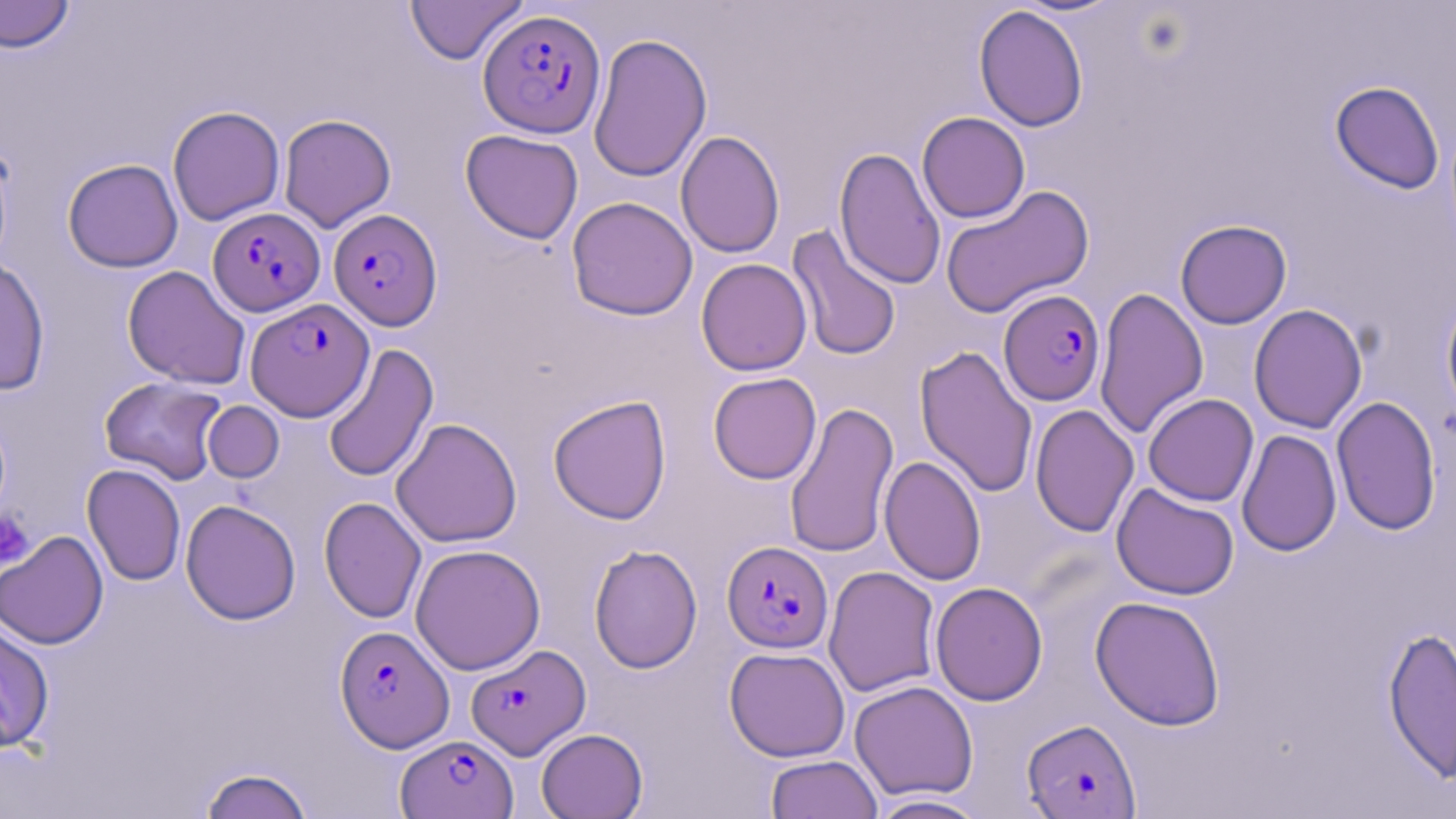 Approximate bounding boxes as named x1/y1/x2/y2 corners in pixels. Plasmodium falciparum-infected red blood cell locations: (x1=478, y1=8, x2=606, y2=138), (x1=208, y1=207, x2=325, y2=316), (x1=328, y1=208, x2=442, y2=330), (x1=998, y1=289, x2=1106, y2=406), (x1=246, y1=298, x2=374, y2=420), (x1=722, y1=540, x2=833, y2=653), (x1=335, y1=625, x2=454, y2=751), (x1=466, y1=644, x2=591, y2=760), (x1=1021, y1=718, x2=1141, y2=818), (x1=395, y1=734, x2=518, y2=819). Uninfected red blood cell locations: (x1=405, y1=0, x2=528, y2=65), (x1=0, y1=1, x2=75, y2=53), (x1=973, y1=5, x2=1088, y2=132), (x1=588, y1=33, x2=712, y2=182), (x1=1330, y1=80, x2=1444, y2=194), (x1=167, y1=105, x2=285, y2=225), (x1=917, y1=111, x2=1030, y2=223), (x1=278, y1=114, x2=396, y2=232), (x1=460, y1=129, x2=584, y2=244), (x1=676, y1=130, x2=785, y2=258), (x1=834, y1=146, x2=946, y2=290), (x1=62, y1=158, x2=183, y2=272), (x1=939, y1=184, x2=1096, y2=319), (x1=566, y1=196, x2=698, y2=321), (x1=1175, y1=219, x2=1292, y2=329), (x1=786, y1=225, x2=902, y2=361), (x1=0, y1=256, x2=50, y2=395), (x1=696, y1=258, x2=812, y2=376), (x1=122, y1=265, x2=251, y2=389), (x1=1095, y1=287, x2=1208, y2=439), (x1=1440, y1=291, x2=1456, y2=422), (x1=1248, y1=303, x2=1367, y2=434), (x1=323, y1=343, x2=438, y2=484), (x1=915, y1=345, x2=1038, y2=498), (x1=708, y1=372, x2=822, y2=484), (x1=99, y1=376, x2=227, y2=485), (x1=1143, y1=393, x2=1259, y2=506), (x1=548, y1=395, x2=672, y2=524), (x1=1331, y1=396, x2=1441, y2=535), (x1=784, y1=400, x2=899, y2=559), (x1=203, y1=401, x2=284, y2=483), (x1=1030, y1=404, x2=1139, y2=537), (x1=390, y1=417, x2=523, y2=548), (x1=1236, y1=429, x2=1342, y2=557), (x1=879, y1=455, x2=986, y2=585), (x1=82, y1=463, x2=186, y2=587), (x1=1111, y1=482, x2=1240, y2=600), (x1=318, y1=496, x2=427, y2=623), (x1=180, y1=498, x2=301, y2=626), (x1=0, y1=530, x2=109, y2=649), (x1=588, y1=543, x2=703, y2=674), (x1=410, y1=544, x2=546, y2=675), (x1=823, y1=565, x2=941, y2=697), (x1=930, y1=582, x2=1048, y2=706), (x1=1090, y1=595, x2=1226, y2=731), (x1=0, y1=619, x2=55, y2=753), (x1=1382, y1=624, x2=1456, y2=785), (x1=724, y1=646, x2=850, y2=762), (x1=849, y1=680, x2=979, y2=801), (x1=535, y1=728, x2=648, y2=819), (x1=765, y1=755, x2=882, y2=819), (x1=197, y1=767, x2=314, y2=818), (x1=867, y1=793, x2=989, y2=818). Platelet locations: (x1=0, y1=509, x2=35, y2=569). Slide-level diagnosis: Plasmodium falciparum. One field of a larger specimen. Thin blood film. Light microscopy. May-Grünwald-Giemsa stain. Image is 1456×819 pixels. 1000x magnification.